Classify this cell by malaria status.
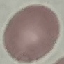

It is uninfected.

Summary:
  - Image type: cell patch, automatically extracted from a larger field of view and resized to 64 × 64 pixels
  - Capture: smartphone through the microscope eyepiece
  - Preparation: thin blood smear
  - Stain: Giemsa